Classify this cell by malaria status.
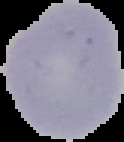

It is uninfected.

From a thin blood film. The area outside the segmented cell region is set to black. Image is 124×142 pixels.